Locate every malaria parasite and every leukocyte.
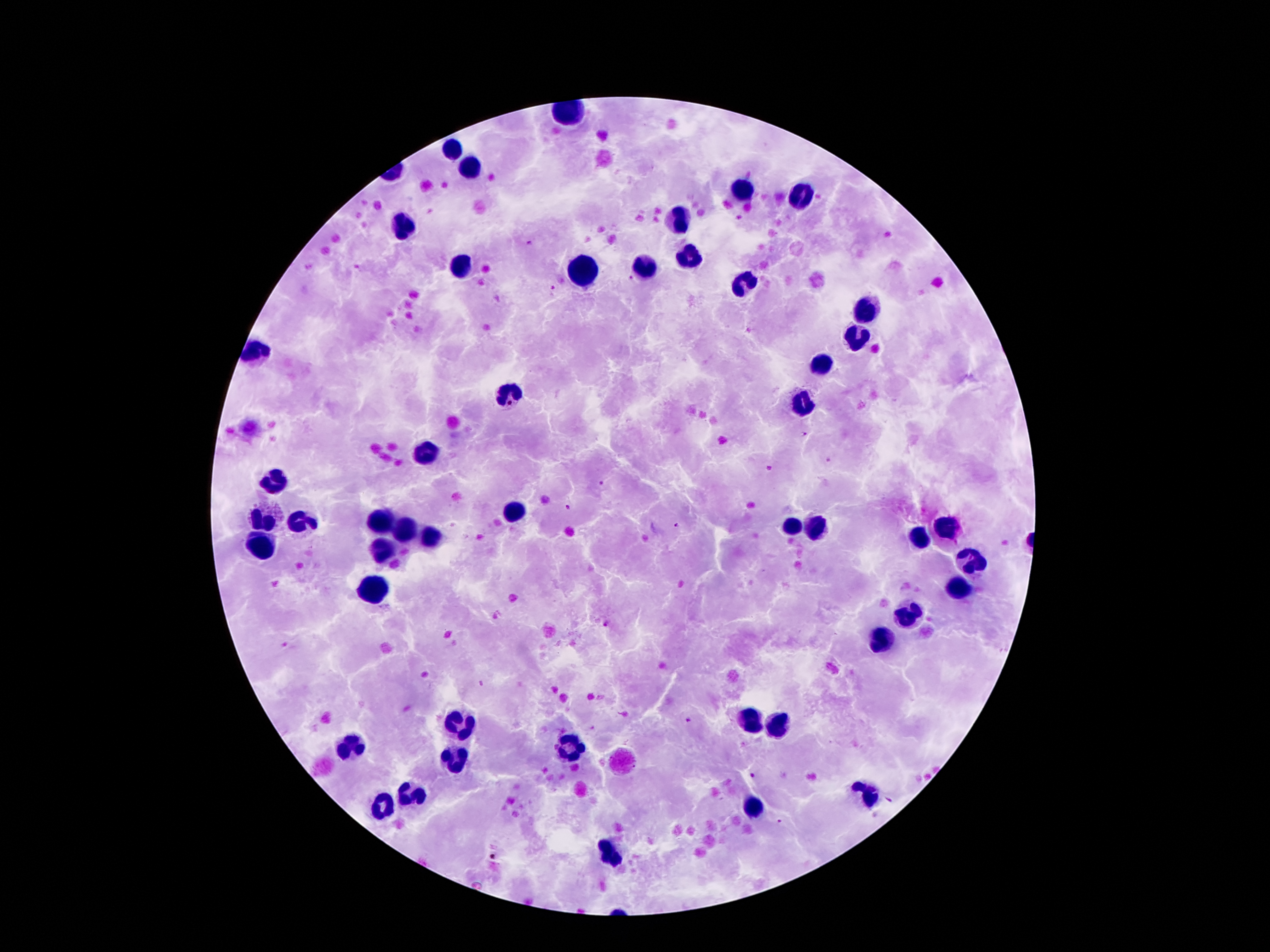

Approximate centers as [x, y] in pixels.
Malaria parasites: [527, 243], [630, 279], [553, 288], [803, 434], [828, 460], [600, 484], [569, 508], [676, 525], [605, 624], [481, 682], [689, 722], [753, 775].
Leukocytes: [452, 151], [470, 169], [740, 191], [806, 197], [677, 222], [404, 227], [688, 256], [461, 266], [645, 267], [586, 274], [747, 284], [868, 311], [854, 334], [252, 354], [818, 365], [504, 397], [804, 404], [425, 452], [277, 478], [513, 513], [261, 518], [302, 520], [384, 522], [795, 524], [947, 527], [404, 531], [815, 531], [434, 537], [917, 542], [263, 545], [386, 549], [972, 563], [956, 590], [372, 592], [906, 617], [883, 640], [452, 721], [746, 721], [775, 727], [353, 747], [569, 748], [454, 759], [867, 794], [412, 795], [380, 808], [756, 810], [615, 856].

Summary:
  - Stain: Giemsa
  - Capture: smartphone camera through the microscope eyepiece
  - Preparation: thick blood smear
  - Patient malaria status: infected with Plasmodium falciparum
  - Field of view: single
  - Image size: 1270×952 pixels
  - Magnification: 100x